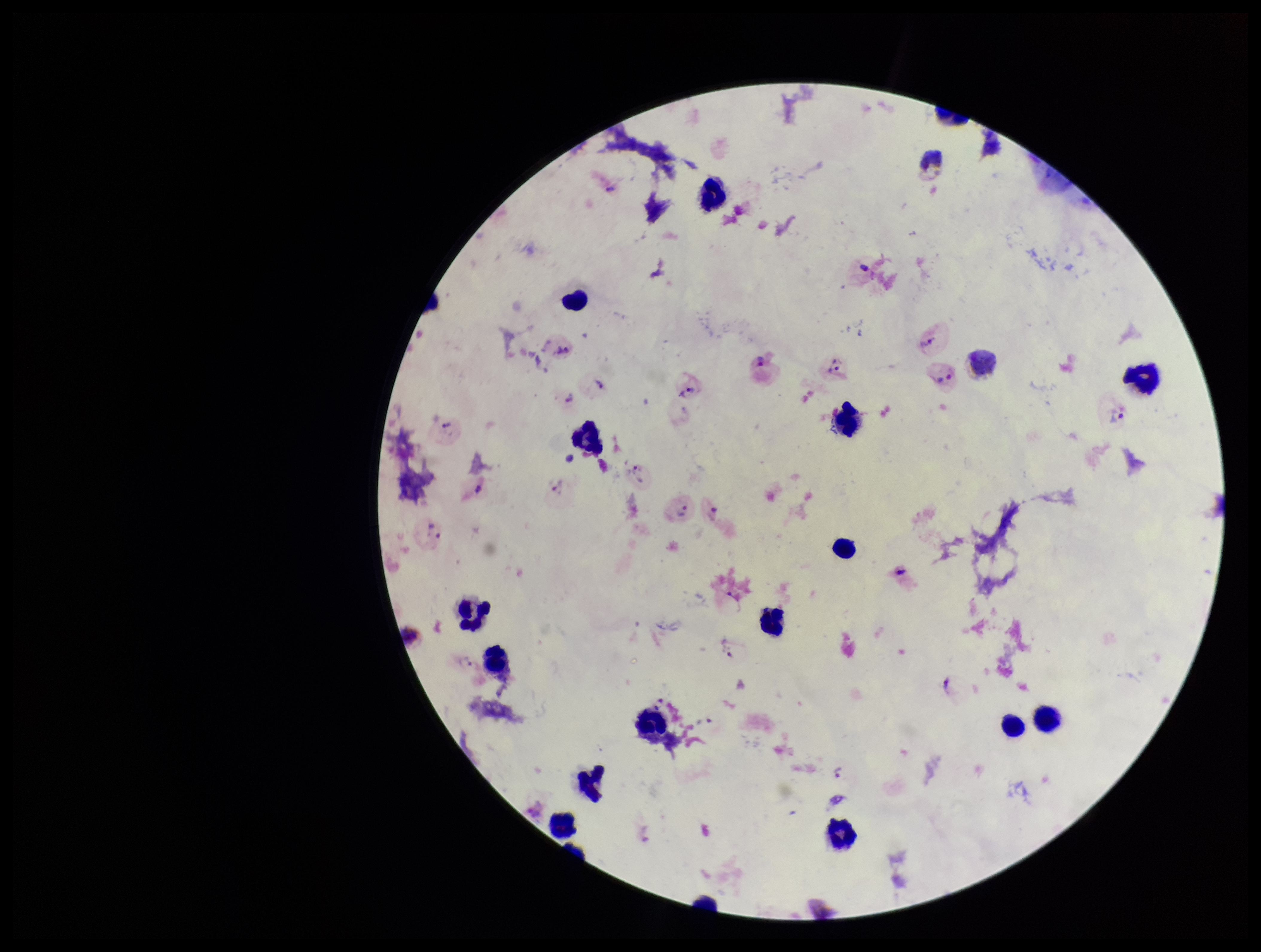 One field from this slide. Leukocyte count: 18. Image is 1261×952 pixels. Parasite count: 19. Preparation: thick blood smear. Plasmodium parasites: detected. Patient malaria status: infected. Giemsa stain. Species reported for this patient: Plasmodium vivax. Smartphone photograph taken through the eyepiece of a microscope.